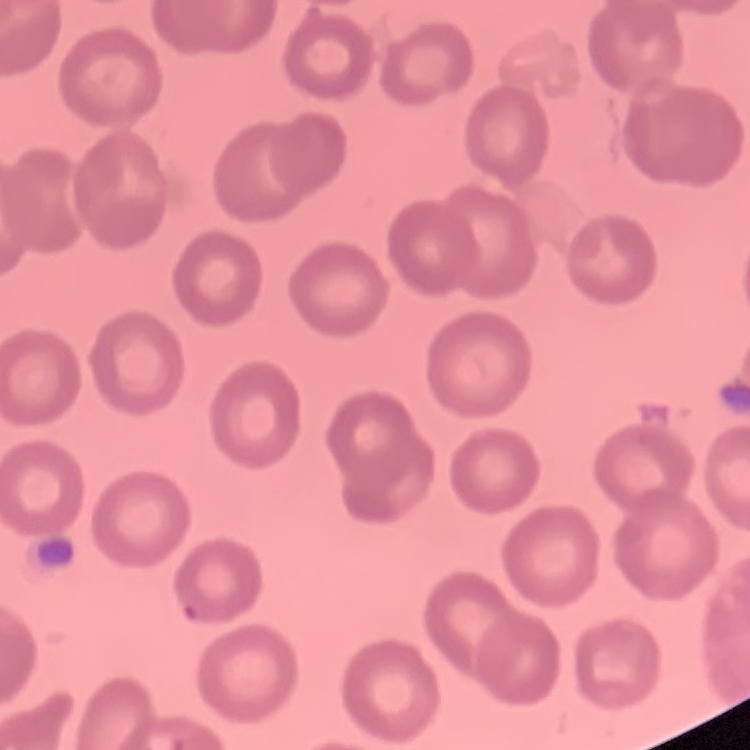

The erythrocytes show no rouleaux formation. One tile cut from a larger photomicrograph. Field's or Giemsa stain. Thin peripheral smear.